Point out each Plasmodium parasite and each leukocyte.
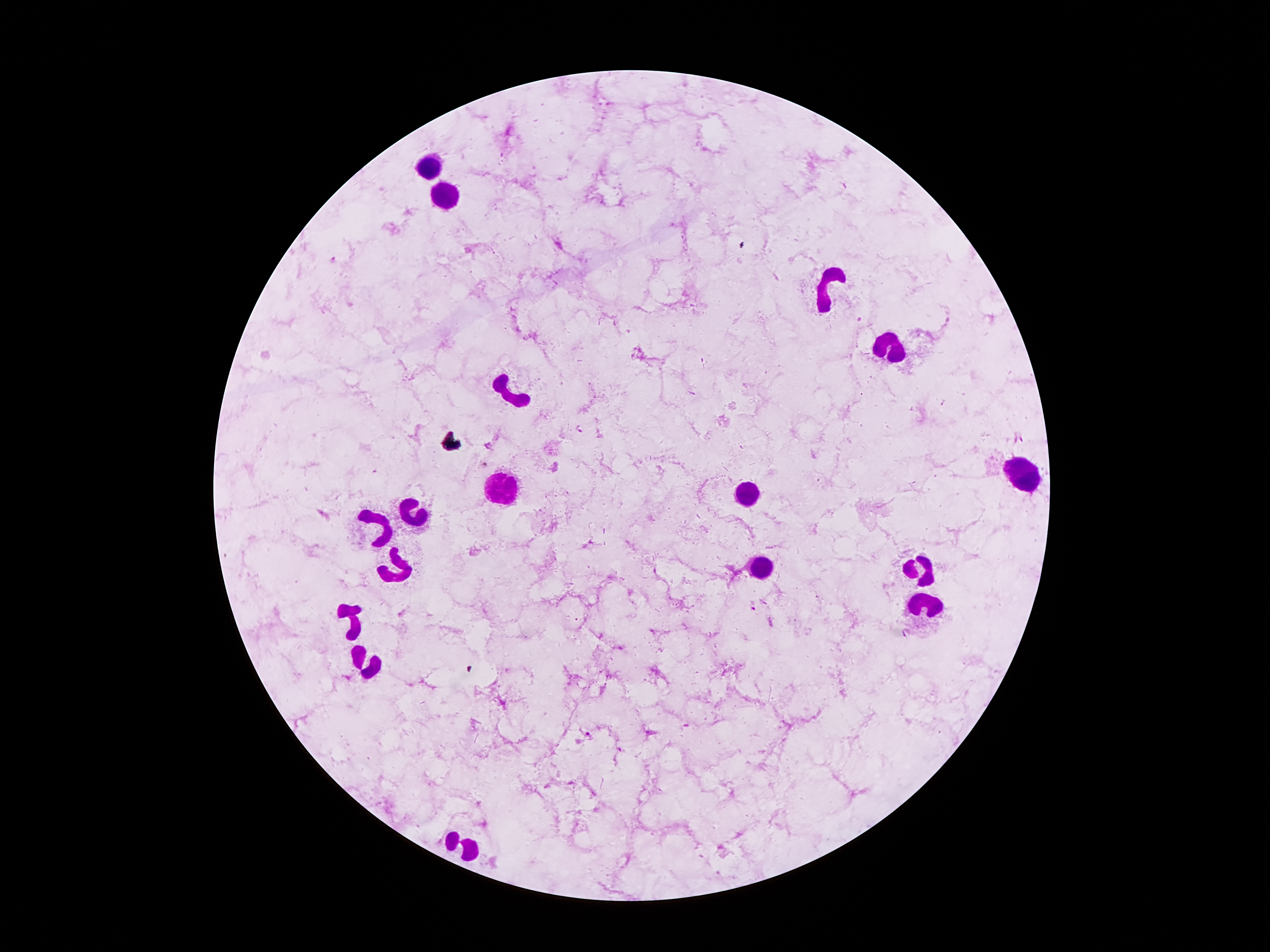

Approximate centers as (x, y) in pixels.
Plasmodium parasites: (333, 258), (580, 429), (485, 465), (753, 606), (588, 734).
Leukocytes: (433, 165), (450, 197), (824, 289), (890, 350), (511, 391), (1020, 475), (502, 490), (752, 493), (412, 507), (381, 525), (765, 566), (400, 568), (920, 568), (926, 604), (349, 614), (364, 666), (465, 847).

Summary:
  - Image size: 1270×952 pixels
  - Capture: smartphone camera through the microscope eyepiece
  - Magnification: 100x
  - Stain: Giemsa
  - Preparation: thick peripheral-blood smear
  - Field of view: one from this slide
  - Patient malaria status: positive for Plasmodium falciparum